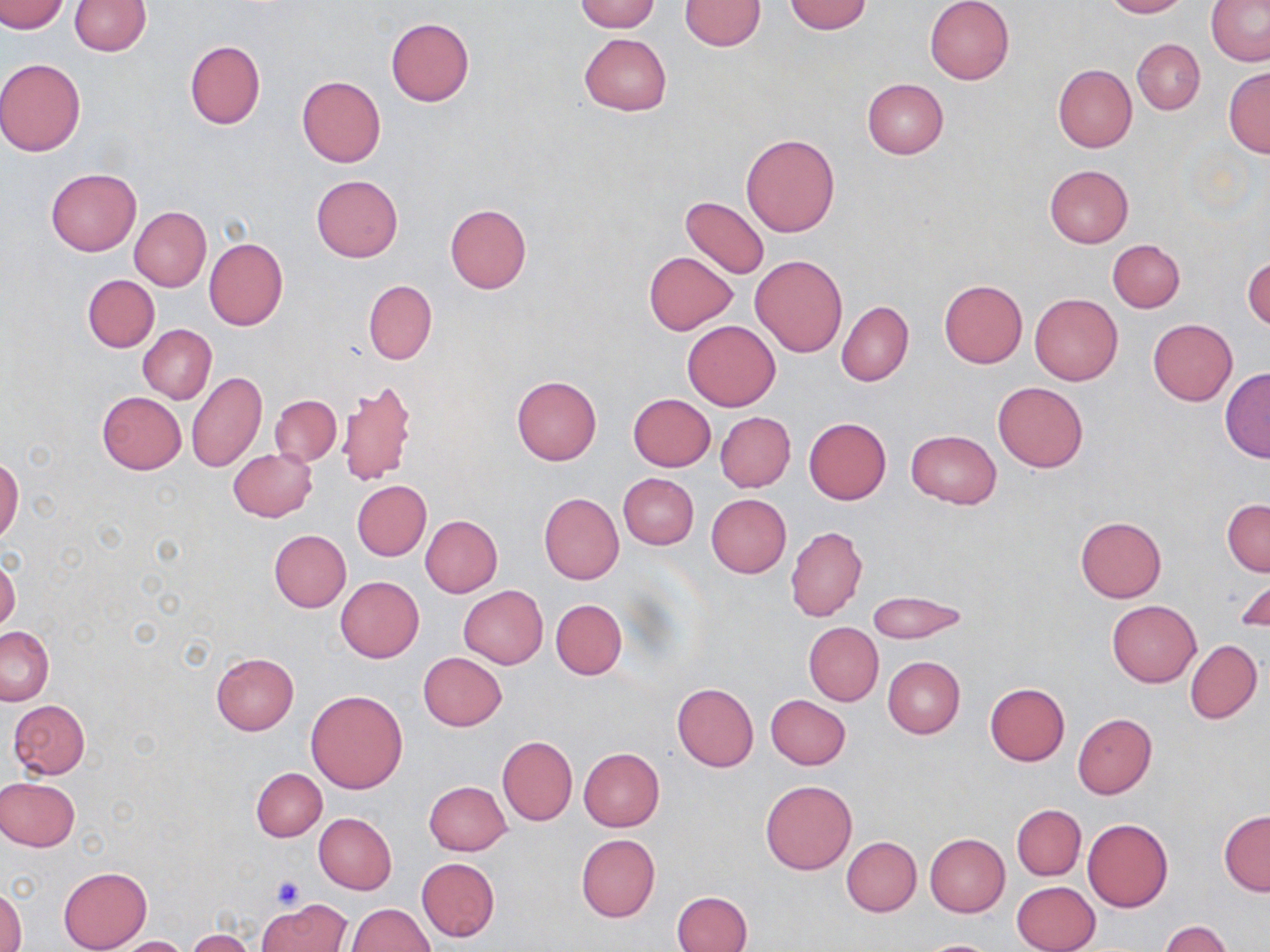

Approximate bounding boxes as (x1,y1)-(x2,y2) corner pairs in pixels. Uninfected red blood cell locations: (0,0)-(67,34), (69,0)-(149,55), (576,0)-(660,32), (678,0)-(766,50), (925,0)-(1015,84), (1102,0)-(1188,18), (782,1)-(872,34), (1205,2)-(1270,66), (386,18)-(475,106), (578,32)-(671,116), (1133,37)-(1205,114), (185,41)-(265,128), (0,59)-(86,157), (1053,64)-(1137,152), (1224,68)-(1269,157), (297,76)-(385,167), (861,79)-(949,159), (740,134)-(840,238), (1044,165)-(1134,248), (45,168)-(141,256), (311,174)-(403,262), (680,196)-(770,279), (444,204)-(531,294), (129,207)-(210,291), (203,238)-(288,330), (1107,239)-(1185,312), (644,250)-(738,335), (1243,253)-(1270,331), (750,255)-(846,357), (83,275)-(159,352), (939,279)-(1027,368), (363,280)-(437,364), (1030,293)-(1122,385), (838,302)-(914,385), (1148,319)-(1237,405), (683,321)-(780,410), (139,324)-(217,403), (1219,367)-(1270,461), (187,371)-(266,472), (510,375)-(602,465), (339,378)-(417,488), (993,382)-(1089,472), (97,391)-(187,474), (628,394)-(716,471), (271,395)-(341,466), (716,411)-(795,492), (803,416)-(891,505), (906,431)-(1001,509), (228,447)-(317,521), (0,457)-(23,544), (618,473)-(698,550), (353,480)-(431,560), (539,493)-(624,583), (706,494)-(792,578), (1222,499)-(1269,576), (420,515)-(502,597), (1074,516)-(1167,602), (786,526)-(867,621), (269,529)-(350,613), (0,559)-(20,631), (1232,574)-(1270,636), (336,577)-(424,662), (459,585)-(548,670), (866,591)-(968,644), (551,599)-(626,680), (1106,599)-(1201,687), (804,622)-(883,705), (0,626)-(53,704), (1186,639)-(1262,724), (418,652)-(508,731), (211,653)-(299,734), (883,656)-(965,738), (672,683)-(759,771), (984,684)-(1069,766), (306,690)-(408,793), (766,694)-(851,769), (8,700)-(90,778), (1073,714)-(1157,799), (497,736)-(576,825), (579,748)-(665,831), (251,767)-(326,841), (0,776)-(80,851), (423,780)-(512,856), (761,780)-(856,874), (1012,804)-(1085,880), (1219,811)-(1270,895), (313,812)-(396,893), (1082,818)-(1174,912), (576,833)-(660,923), (924,833)-(1010,917), (842,837)-(921,916), (417,858)-(499,942), (58,866)-(152,951), (1012,880)-(1100,952), (0,888)-(25,952), (673,891)-(753,952), (259,900)-(351,952), (346,903)-(435,951), (1160,920)-(1232,952), (189,930)-(257,952), (116,936)-(190,952), (917,939)-(1002,952). Platelet locations: (270,874)-(306,909). Slide-level diagnosis: no evidence of blood parasites. One field of a larger specimen. Thin blood smear. Captured at 1000x magnification. Image is 1270×952 pixels. May-Grünwald-Giemsa-stained preparation. Optical microscopy.